Identify the preparation type.
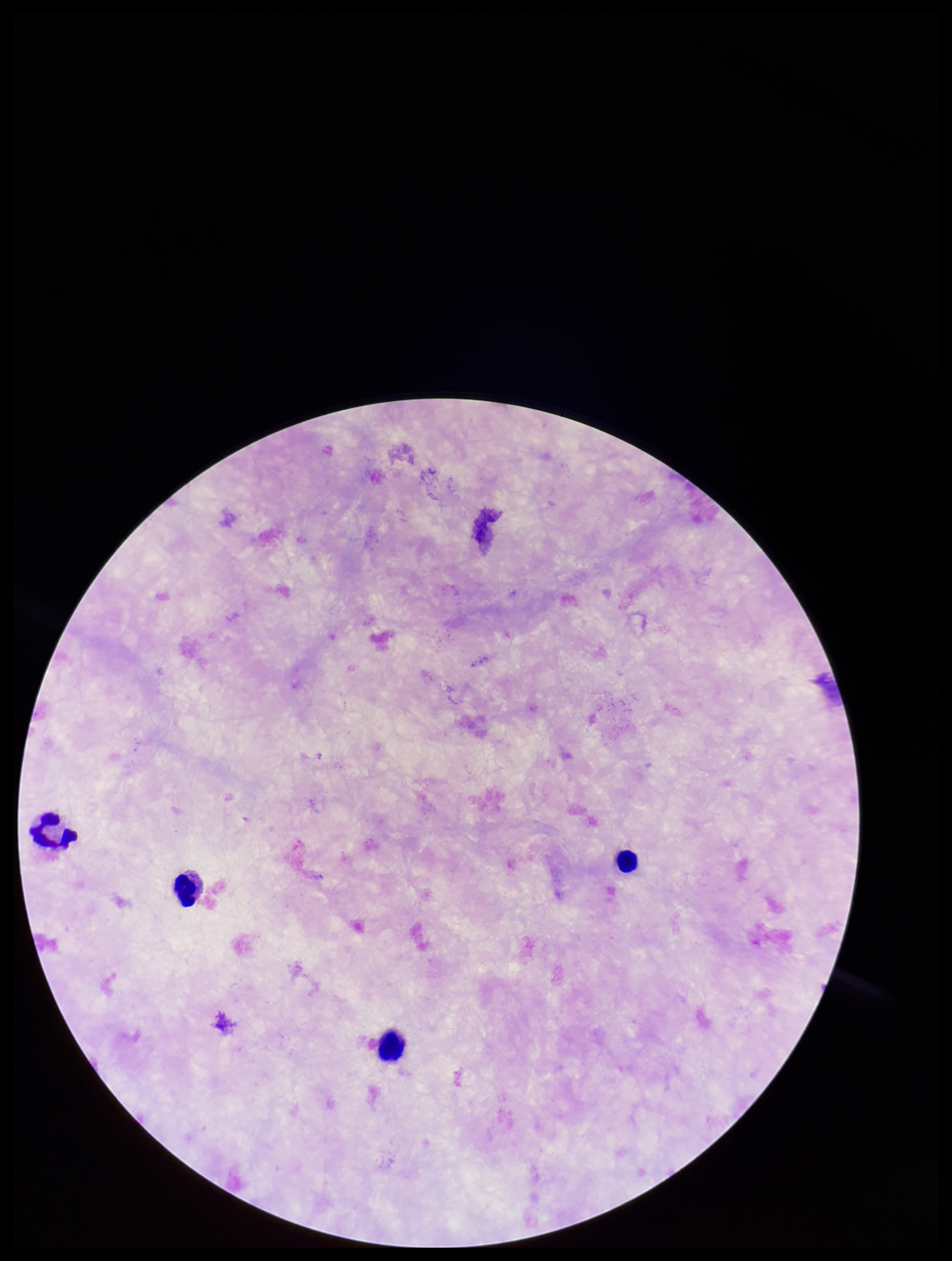
Thick.

Plasmodium parasites = none seen
capture = smartphone photograph through the microscope eyepiece
field of view = single
parasite count = 0
leukocyte count = 4
patient malaria status = negative
stain = Giemsa
image size = 952×1261 pixels